Assess this cell for malaria.
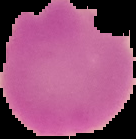
It is uninfected.

Summary:
  - Image type: segmented cell region on a black background
  - Preparation: thin blood film
  - Image size: 136×139 pixels